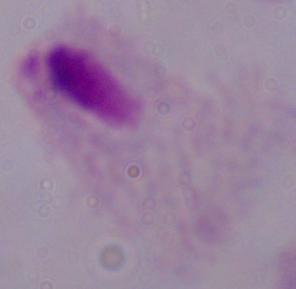

modality = photomicrograph
identification = trichomonad
magnification = 1000x